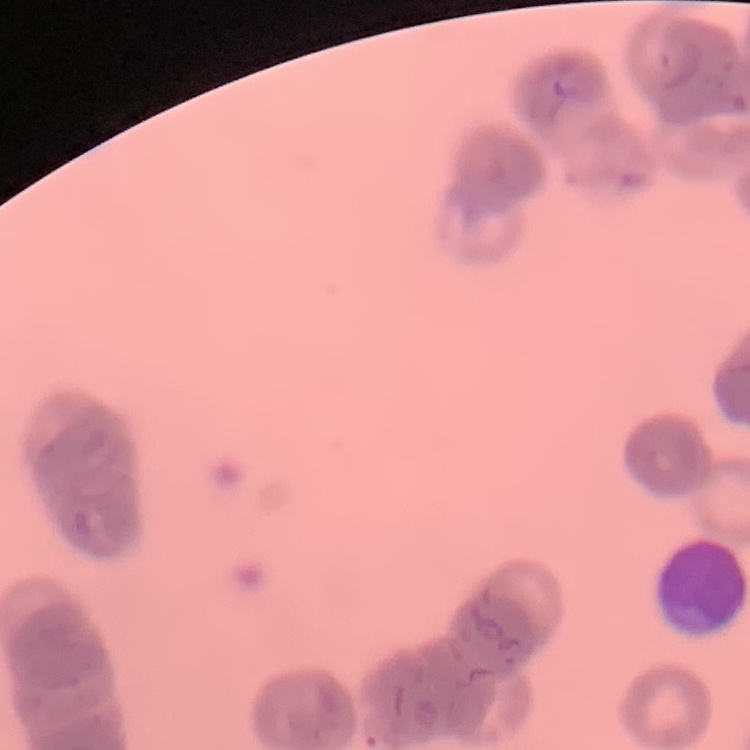

red_blood_cell_morphology: rouleaux formation
preparation: thin peripheral smear
stain: Field's or Giemsa
image_type: square crop of a larger photomicrograph